Classify this cell by malaria status.
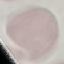
It is uninfected.

Photographed with a smartphone camera at the microscope eyepiece. Giemsa stain. Thin smear of blood. Automatically extracted cell patch, resized to 64 × 64 pixels.